Locate every white blood cell.
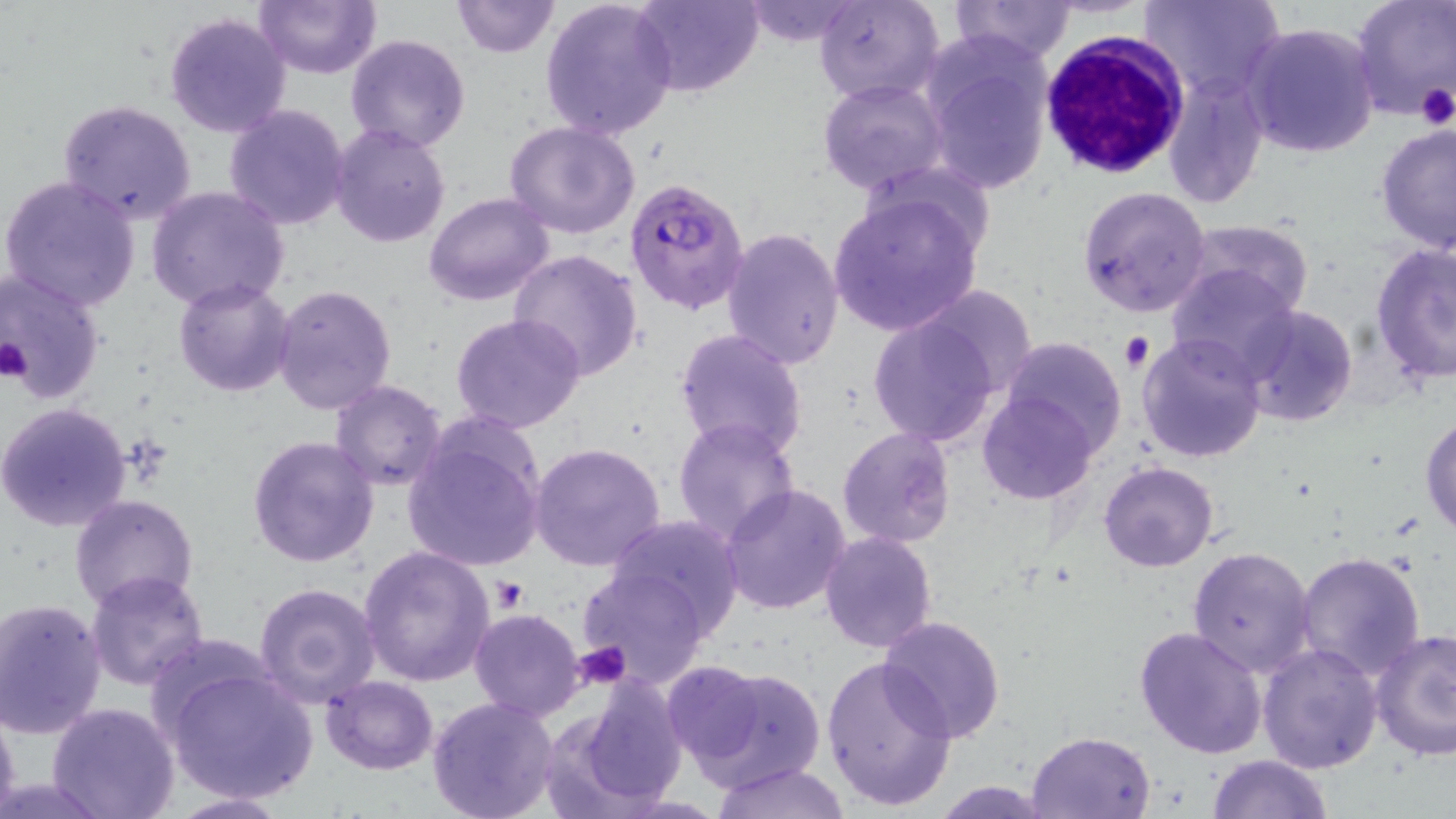

Approximate bounding boxes as [x1, y1, x2, y2] in pixels.
White blood cells: [1040, 31, 1189, 183].

Summary:
  - Uninfected red blood cell locations: [252, 0, 383, 80], [451, 0, 559, 57], [540, 0, 677, 141], [630, 0, 763, 96], [737, 0, 868, 47], [815, 0, 946, 105], [950, 0, 1077, 65], [1141, 0, 1285, 103], [1351, 1, 1455, 121], [164, 11, 291, 137], [1240, 21, 1380, 158], [345, 34, 472, 153], [921, 44, 1053, 194], [1162, 75, 1267, 208], [817, 79, 948, 196], [56, 99, 199, 226], [222, 104, 351, 230], [503, 122, 642, 239], [329, 124, 451, 248], [1376, 124, 1456, 253], [1, 175, 143, 311], [1078, 185, 1211, 319], [146, 186, 291, 311], [828, 191, 985, 337], [424, 192, 554, 306], [1181, 218, 1313, 315], [720, 228, 844, 371], [1371, 243, 1456, 382], [509, 248, 645, 380], [1167, 261, 1299, 376], [0, 272, 106, 399], [173, 277, 295, 396], [273, 284, 398, 414], [917, 286, 1036, 398], [1240, 305, 1356, 427], [869, 312, 1001, 447], [450, 314, 588, 435], [674, 328, 808, 462], [1136, 333, 1267, 463], [1000, 335, 1129, 455], [329, 380, 447, 491], [978, 391, 1096, 503], [0, 403, 132, 532], [1420, 410, 1456, 539], [672, 416, 802, 544], [403, 420, 547, 573], [837, 426, 956, 548], [246, 435, 379, 569], [530, 443, 666, 573], [1098, 461, 1218, 572], [721, 482, 851, 615], [70, 493, 199, 611], [606, 513, 745, 635], [820, 532, 937, 654], [359, 545, 494, 687], [1188, 546, 1316, 678], [1295, 551, 1426, 682], [576, 565, 712, 689], [86, 570, 211, 692], [253, 581, 382, 706], [0, 600, 107, 738], [469, 608, 585, 720], [876, 615, 1005, 743], [1134, 625, 1268, 759], [1371, 628, 1456, 761], [1257, 642, 1383, 773], [821, 655, 956, 811], [663, 660, 767, 768], [165, 664, 319, 804], [683, 664, 827, 791], [319, 675, 438, 774], [558, 680, 688, 810], [427, 696, 560, 819], [47, 702, 181, 819], [0, 704, 21, 819], [1026, 730, 1154, 819], [1206, 753, 1334, 818], [713, 761, 848, 819], [932, 779, 1049, 817], [165, 792, 292, 818]
  - Platelet locations: [1414, 82, 1456, 128], [1118, 331, 1154, 372], [0, 337, 32, 381], [491, 578, 528, 611], [576, 641, 630, 689]
  - Plasmodium falciparum-infected red blood cell locations: [623, 175, 751, 317]
  - Slide-level diagnosis: Plasmodium falciparum
  - Stain: May-Grünwald-Giemsa
  - Modality: light microscopy
  - Preparation: thin blood film
  - Field of view: one of a larger specimen
  - Image size: 1456×819 pixels
  - Magnification: 1000x